Report the malaria status of this cell.
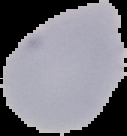

It is uninfected.

Summary:
  - Preparation: thin blood film
  - Image type: segmented cell region on a black background
  - Image size: 127×136 pixels